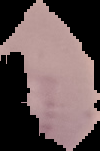 From a thin blood smear. The area outside the segmented cell region is set to black. Result: Plasmodium parasites identified. Image is 100×151 pixels.